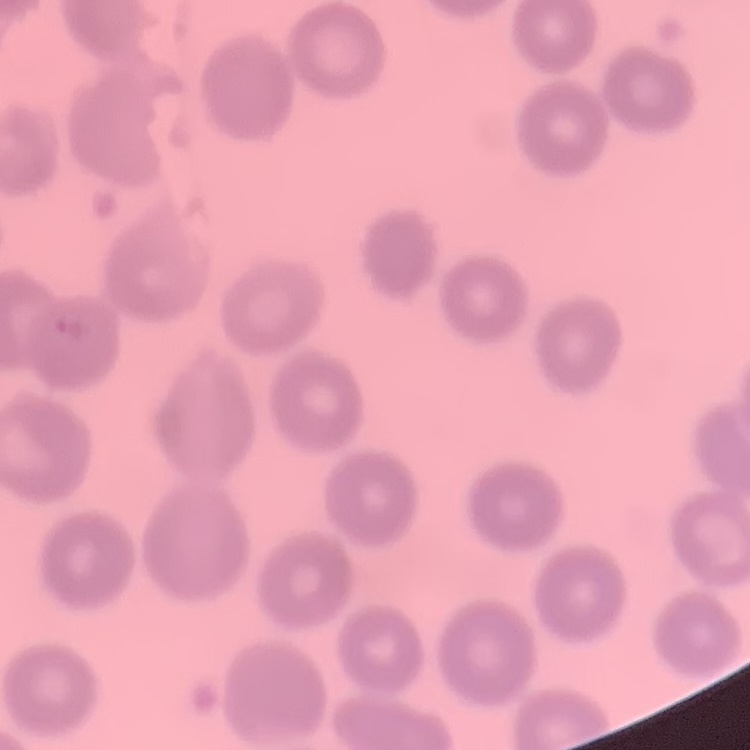

Summary:
  - Red blood cell morphology: no rouleaux formation
  - Stain: Field's or Giemsa
  - Image type: square crop of a larger photomicrograph
  - Preparation: thin blood smear